Locate every blood parasite and identify its species.
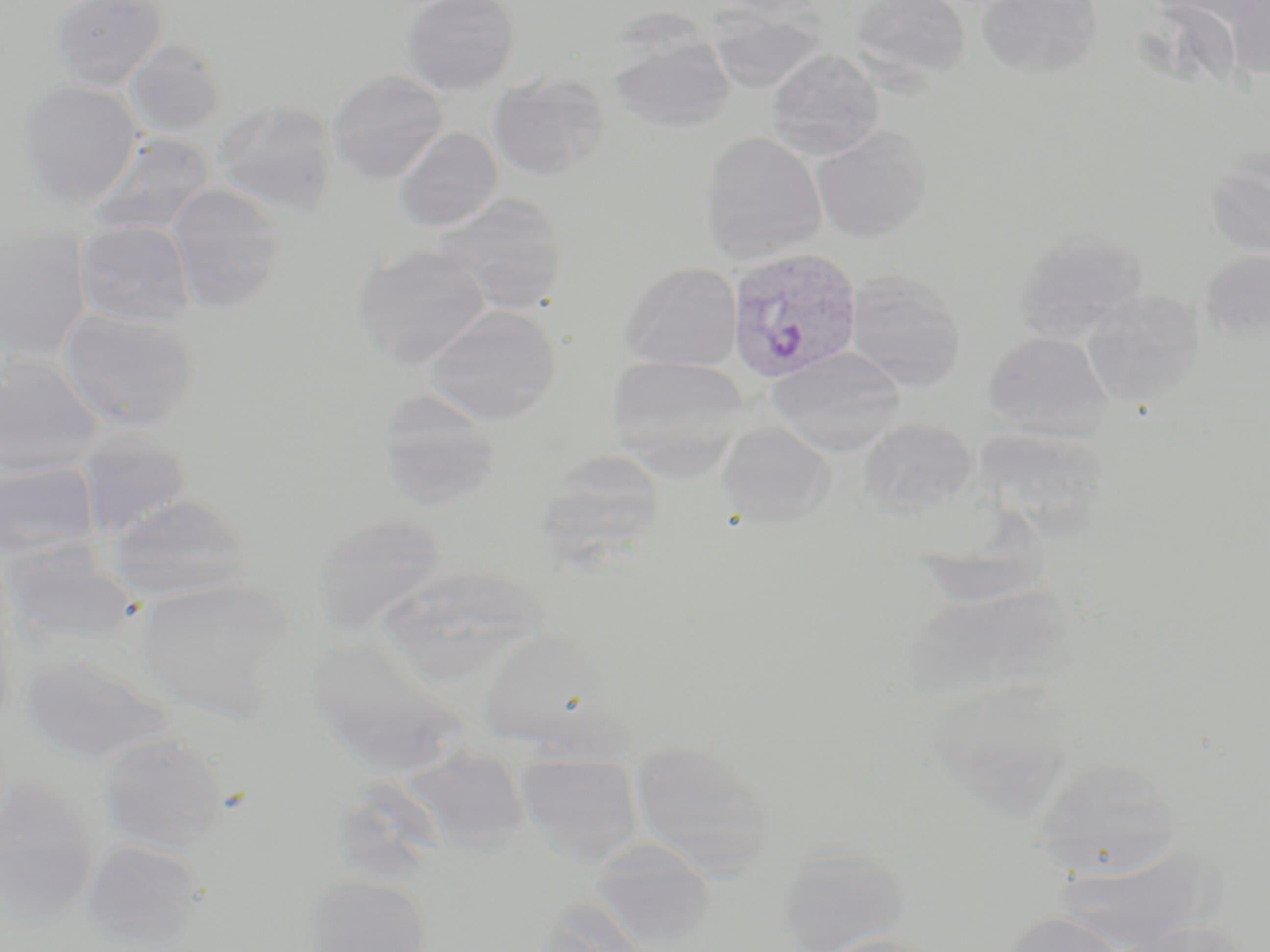
Approximate bounding boxes as (x1, y1, x2, y2) in pixels.
Plasmodium vivax-infected red blood cells: (727, 246, 861, 384).
No Plasmodium falciparum, Plasmodium ovale, Plasmodium malariae, Babesia divergens, or Trypanosoma brucei observed.

{
  "slide_level_diagnosis": "Plasmodium vivax",
  "field_of_view": "one of a larger specimen",
  "uninfected_red_blood_cell_locations": "approximate bounding boxes as (x1, y1, x2, y2) in pixels: (49, 0, 167, 90), (401, 0, 519, 95), (847, 0, 971, 83), (978, 0, 1102, 78), (1227, 0, 1270, 80), (707, 9, 826, 92), (608, 33, 735, 132), (127, 40, 226, 135), (767, 49, 884, 159), (328, 70, 448, 184), (488, 74, 609, 180), (18, 79, 143, 205), (214, 100, 339, 217), (394, 127, 502, 232), (812, 127, 932, 241), (700, 132, 827, 261), (88, 133, 215, 236), (1204, 156, 1270, 262), (167, 184, 284, 312), (433, 194, 568, 313), (75, 220, 196, 326), (1015, 231, 1149, 340), (0, 233, 92, 361), (352, 244, 491, 369), (1200, 249, 1270, 342), (620, 262, 741, 370), (844, 271, 966, 391), (1081, 289, 1205, 407), (422, 304, 562, 425), (58, 308, 200, 430), (983, 331, 1113, 438), (766, 346, 906, 456), (0, 354, 102, 477), (605, 355, 750, 475), (377, 390, 503, 509), (858, 418, 978, 515), (716, 422, 835, 529), (976, 430, 1120, 553), (77, 436, 193, 540), (547, 448, 667, 573), (0, 459, 101, 563), (104, 492, 253, 601), (311, 514, 448, 634), (910, 555, 1057, 608), (389, 568, 552, 682), (132, 577, 293, 725), (899, 582, 1083, 709), (479, 627, 612, 749), (315, 633, 467, 768), (20, 652, 172, 764), (925, 680, 1079, 817), (97, 732, 229, 852), (628, 738, 771, 864), (399, 746, 531, 854), (515, 751, 644, 862), (1030, 757, 1184, 880), (0, 777, 101, 925), (80, 838, 208, 949), (776, 847, 910, 952), (301, 874, 434, 952), (529, 908, 651, 952), (1002, 912, 1128, 952), (1111, 919, 1252, 952), (809, 932, 947, 952)",
  "preparation": "thin blood smear",
  "magnification": "1000x",
  "modality": "optical microscopy",
  "stain": "May-Grünwald-Giemsa",
  "image_size": "1270×952 pixels"
}